Locate every blood parasite and identify its species.
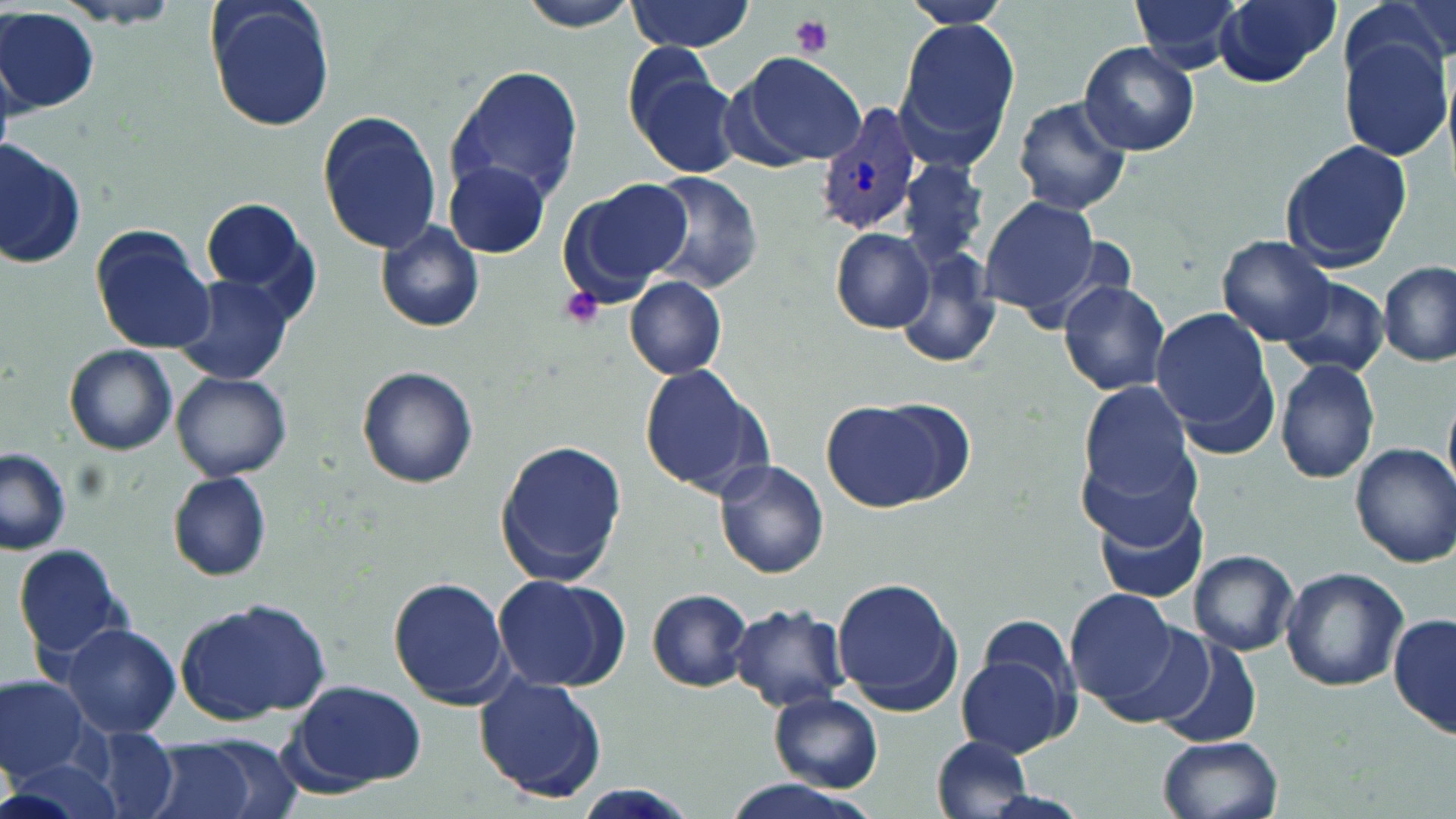

Approximate bounding boxes as [x1, y1, x2, y2] in pixels.
Plasmodium vivax-infected red blood cells: [818, 101, 920, 236].
No Plasmodium falciparum, Plasmodium ovale, Plasmodium malariae, Babesia divergens, or Trypanosoma brucei observed.

{
  "slide_level_diagnosis": "Plasmodium vivax",
  "modality": "optical microscopy",
  "field_of_view": "single",
  "magnification": "1000x",
  "image_size": "1456×819 pixels",
  "stain": "May-Grünwald-Giemsa",
  "uninfected_red_blood_cell_locations": "approximate bounding boxes as [x1, y1, x2, y2] in pixels: [204, 0, 336, 134], [509, 0, 648, 31], [905, 0, 1010, 29], [1131, 0, 1244, 70], [1214, 0, 1341, 86], [1347, 0, 1454, 86], [625, 2, 758, 52], [0, 7, 97, 113], [893, 16, 1021, 165], [1339, 36, 1454, 160], [1079, 41, 1200, 157], [734, 51, 867, 167], [628, 54, 742, 178], [444, 63, 585, 204], [1011, 96, 1131, 216], [316, 110, 442, 253], [1279, 136, 1414, 272], [1, 138, 86, 272], [901, 156, 988, 268], [444, 161, 551, 258], [646, 174, 762, 294], [557, 178, 692, 304], [199, 196, 320, 320], [978, 197, 1099, 316], [375, 222, 483, 333], [90, 224, 216, 355], [830, 227, 934, 333], [1215, 235, 1337, 347], [896, 241, 1004, 369], [1379, 260, 1453, 365], [174, 274, 298, 388], [625, 276, 728, 381], [1279, 277, 1388, 376], [1058, 279, 1172, 396], [1149, 308, 1276, 439], [64, 344, 178, 456], [1275, 356, 1380, 484], [639, 363, 771, 499], [356, 365, 479, 490], [171, 372, 291, 481], [1076, 379, 1195, 503], [820, 397, 957, 514], [1079, 438, 1201, 551], [493, 440, 627, 585], [1350, 442, 1455, 568], [0, 448, 71, 555], [713, 460, 830, 579], [168, 472, 274, 581], [1095, 498, 1211, 605], [11, 545, 130, 664], [1188, 549, 1298, 656], [1280, 567, 1409, 691], [490, 572, 630, 692], [387, 575, 513, 709], [833, 577, 962, 716], [648, 587, 755, 693], [1066, 588, 1179, 705], [173, 598, 333, 725], [727, 602, 850, 711], [1389, 612, 1454, 741], [58, 621, 181, 739], [1152, 635, 1265, 751], [958, 637, 1076, 758], [474, 675, 609, 804], [1, 676, 90, 781], [283, 679, 429, 794], [768, 691, 884, 792], [82, 728, 181, 819], [1159, 735, 1283, 819], [930, 736, 1032, 818], [141, 737, 270, 819], [6, 754, 123, 819], [568, 785, 697, 817]",
  "platelet_locations": "approximate bounding boxes as [x1, y1, x2, y2] in pixels: [791, 13, 836, 57], [560, 286, 605, 328]",
  "preparation": "thin blood film"
}